Assess the morphology of the erythrocytes.
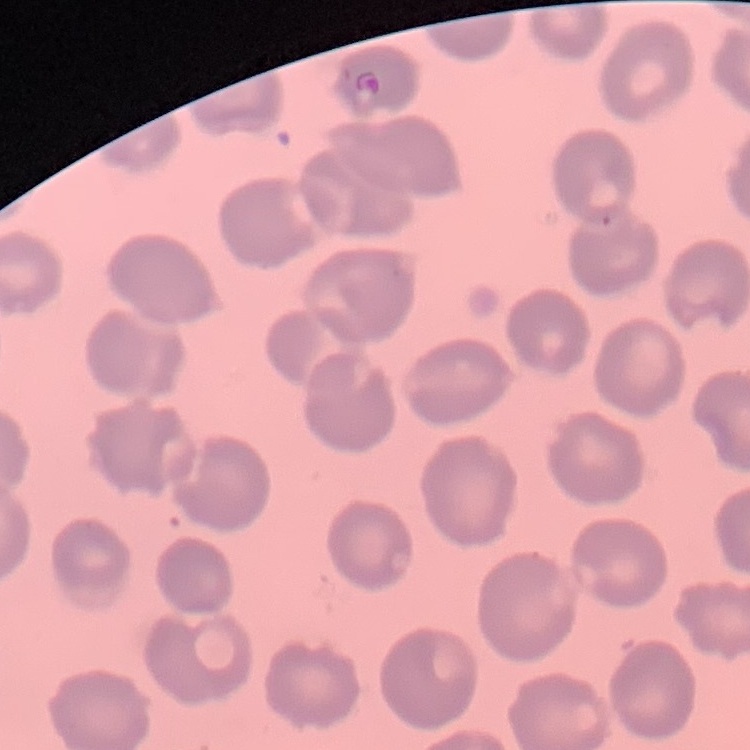
No rouleaux formation.

Summary:
  - Stain: Field's or Giemsa
  - Preparation: thin blood film
  - Image type: square crop of a larger photomicrograph